Assess this cell for malaria.
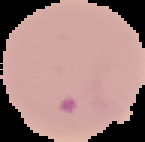

Parasitized.

Image is 145×142 pixels. From a thin blood film. Segmented cell region on a black background.